Assess the morphology of the erythrocytes.
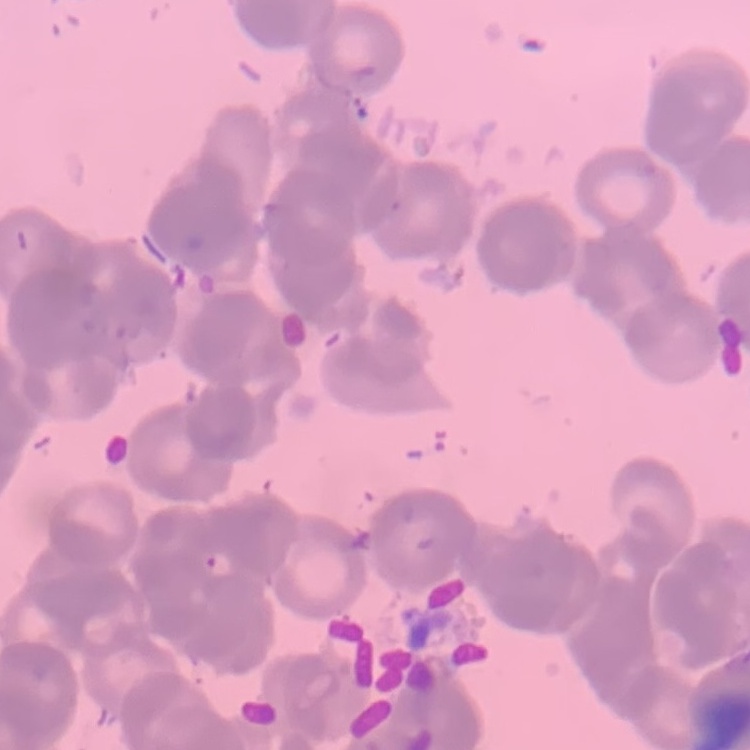
They show rouleaux formation.

image_type: one tile cut from a larger photomicrograph
preparation: thin blood smear
stain: Field's or Giemsa